Assess this cell for malaria.
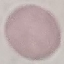

Uninfected.

Summary:
  - Preparation: thin blood film
  - Stain: Giemsa
  - Capture: smartphone camera at the microscope eyepiece
  - Image type: automatically extracted cell patch, resized to 64 × 64 pixels